Assess the morphology of the erythrocytes.
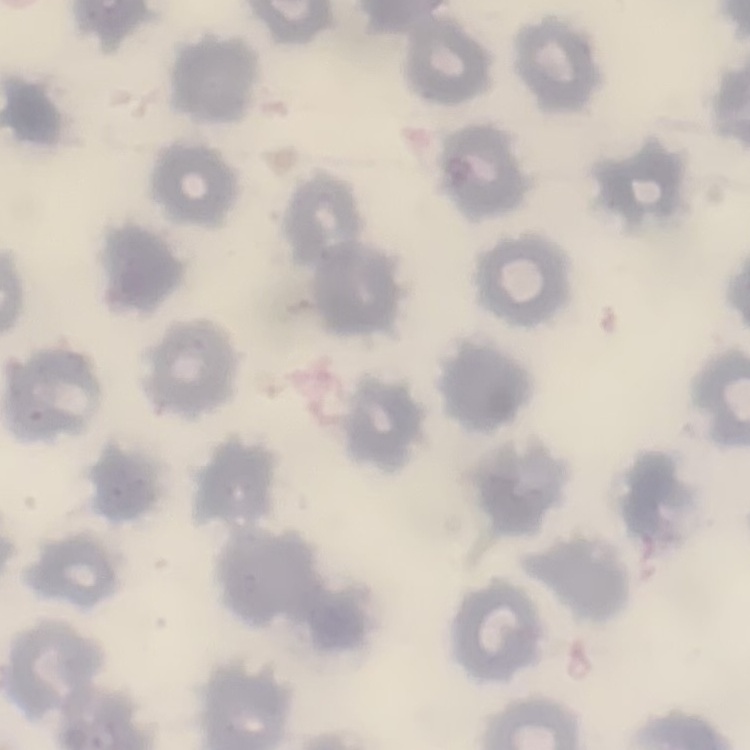

They show no rouleaux formation.

image type = one tile cut from a larger photomicrograph
stain = Field's or Giemsa
preparation = thin blood film